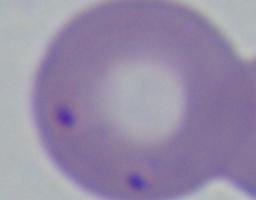

Summary:
  - Modality: photomicrograph
  - Identification: Babesia
  - Magnification: 1000x